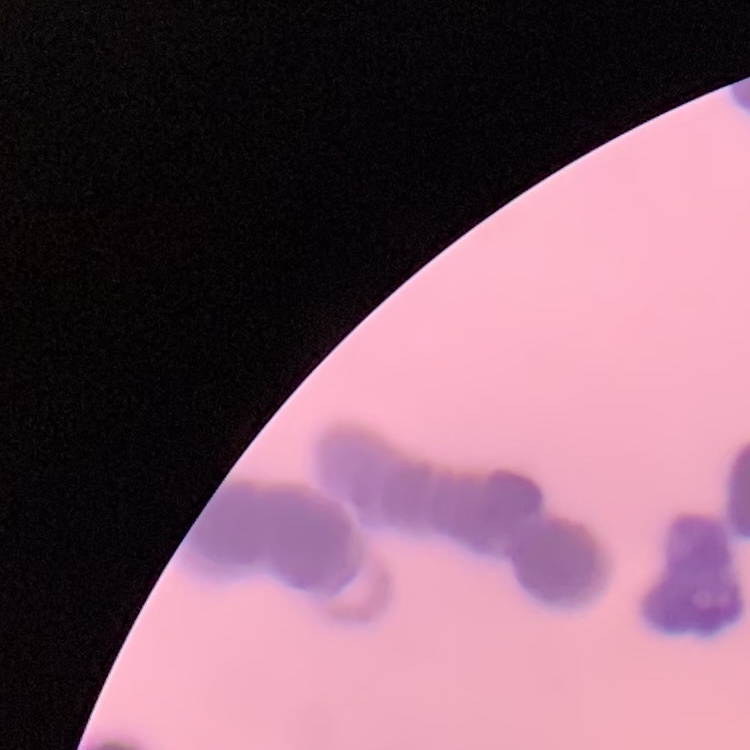
The red blood cells exhibit rouleaux formation. Field's or Giemsa stain. Square crop of a larger photomicrograph. Thin peripheral smear.